Assess this cell for malaria.
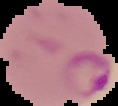

It is parasitized.

The area outside the segmented cell region is set to black. Image is 118×106 pixels. From a thin blood smear.